Locate and identify every blood parasite.
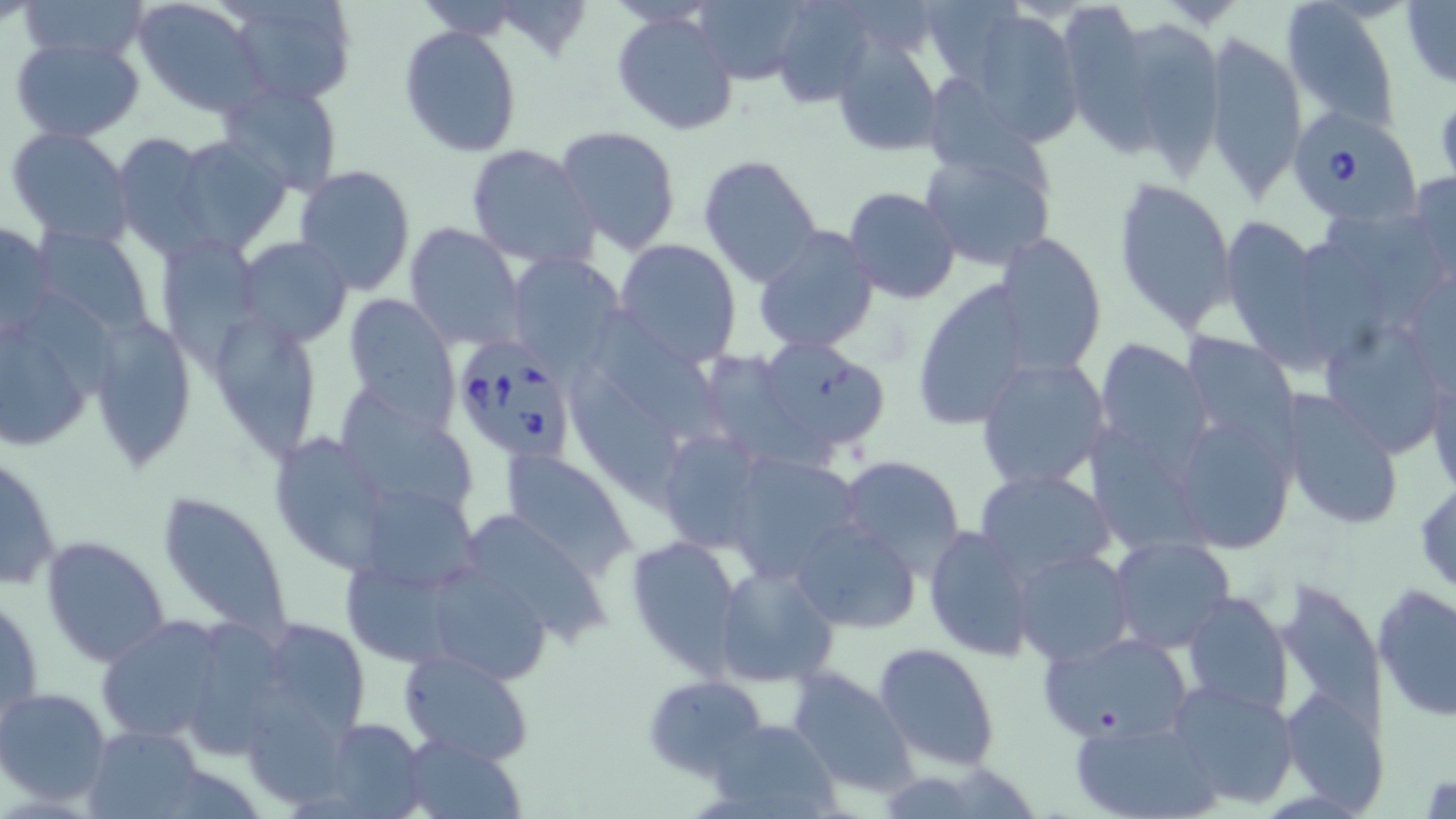
Approximate bounding boxes as [x1, y1, x2, y2] in pixels.
Babesia divergens-infected red blood cells: [1285, 105, 1421, 226], [459, 342, 570, 469].
No Plasmodium falciparum, Plasmodium ovale, Plasmodium malariae, Plasmodium vivax, or Trypanosoma brucei observed.

slide-level diagnosis = Babesia divergens
preparation = thin blood smear
magnification = 1000x
stain = May-Grünwald-Giemsa
modality = light microscopy
image size = 1456×819 pixels
uninfected red blood cell locations = approximate bounding boxes as [x1, y1, x2, y2] in pixels: [16, 0, 150, 64], [131, 0, 269, 116], [223, 0, 359, 109], [773, 0, 876, 107], [1280, 0, 1401, 134], [689, 2, 811, 87], [1401, 2, 1456, 89], [1057, 7, 1154, 159], [613, 9, 741, 136], [968, 9, 1084, 147], [399, 25, 523, 157], [1203, 29, 1307, 202], [1129, 30, 1229, 181], [9, 34, 146, 142], [830, 36, 946, 160], [218, 81, 345, 195], [927, 83, 1055, 202], [555, 125, 682, 255], [7, 128, 133, 245], [109, 132, 219, 255], [163, 135, 290, 257], [466, 143, 602, 272], [921, 143, 1056, 269], [698, 154, 824, 289], [294, 165, 417, 297], [1404, 171, 1456, 278], [1112, 176, 1237, 332], [843, 186, 960, 303], [1324, 213, 1449, 322], [1224, 215, 1340, 381], [1, 217, 56, 345], [404, 222, 527, 353], [752, 225, 879, 353], [33, 226, 153, 339], [994, 231, 1109, 373], [154, 234, 262, 360], [234, 237, 353, 348], [613, 237, 743, 367], [1303, 248, 1382, 372], [503, 252, 623, 369], [909, 276, 1037, 430], [340, 292, 462, 426], [0, 301, 105, 451], [596, 307, 733, 446], [208, 309, 325, 460], [86, 312, 197, 471], [1324, 324, 1447, 462], [1181, 327, 1307, 476], [743, 337, 893, 460], [1093, 340, 1211, 470], [712, 353, 832, 470], [974, 358, 1108, 494], [560, 360, 691, 514], [1425, 360, 1455, 500], [338, 388, 485, 512], [1278, 389, 1404, 533], [1167, 408, 1300, 555], [266, 427, 401, 573], [1095, 429, 1209, 560], [653, 432, 767, 556], [501, 449, 638, 578], [722, 452, 864, 584], [0, 453, 61, 596], [837, 455, 967, 574], [975, 469, 1113, 582], [1415, 479, 1456, 599], [354, 484, 481, 591], [157, 489, 296, 641], [467, 512, 609, 645], [794, 520, 921, 634], [923, 525, 1037, 662], [624, 534, 742, 673], [1108, 535, 1236, 652], [40, 536, 171, 668], [1014, 548, 1135, 665], [340, 563, 459, 671], [715, 564, 839, 687], [437, 571, 557, 686], [1374, 584, 1456, 722], [2, 588, 43, 733], [1183, 592, 1293, 713], [95, 614, 236, 747], [195, 619, 292, 759], [272, 625, 368, 733], [1039, 631, 1194, 745], [873, 641, 1000, 770], [396, 648, 536, 767], [787, 666, 918, 799], [643, 676, 767, 781], [240, 679, 341, 803], [1166, 679, 1299, 809], [1278, 686, 1387, 812], [0, 687, 112, 807], [1071, 716, 1221, 819], [709, 718, 840, 818], [315, 719, 429, 815], [83, 724, 206, 817], [399, 733, 528, 819]
field of view = one of a larger specimen